Locate and identify every blood parasite.
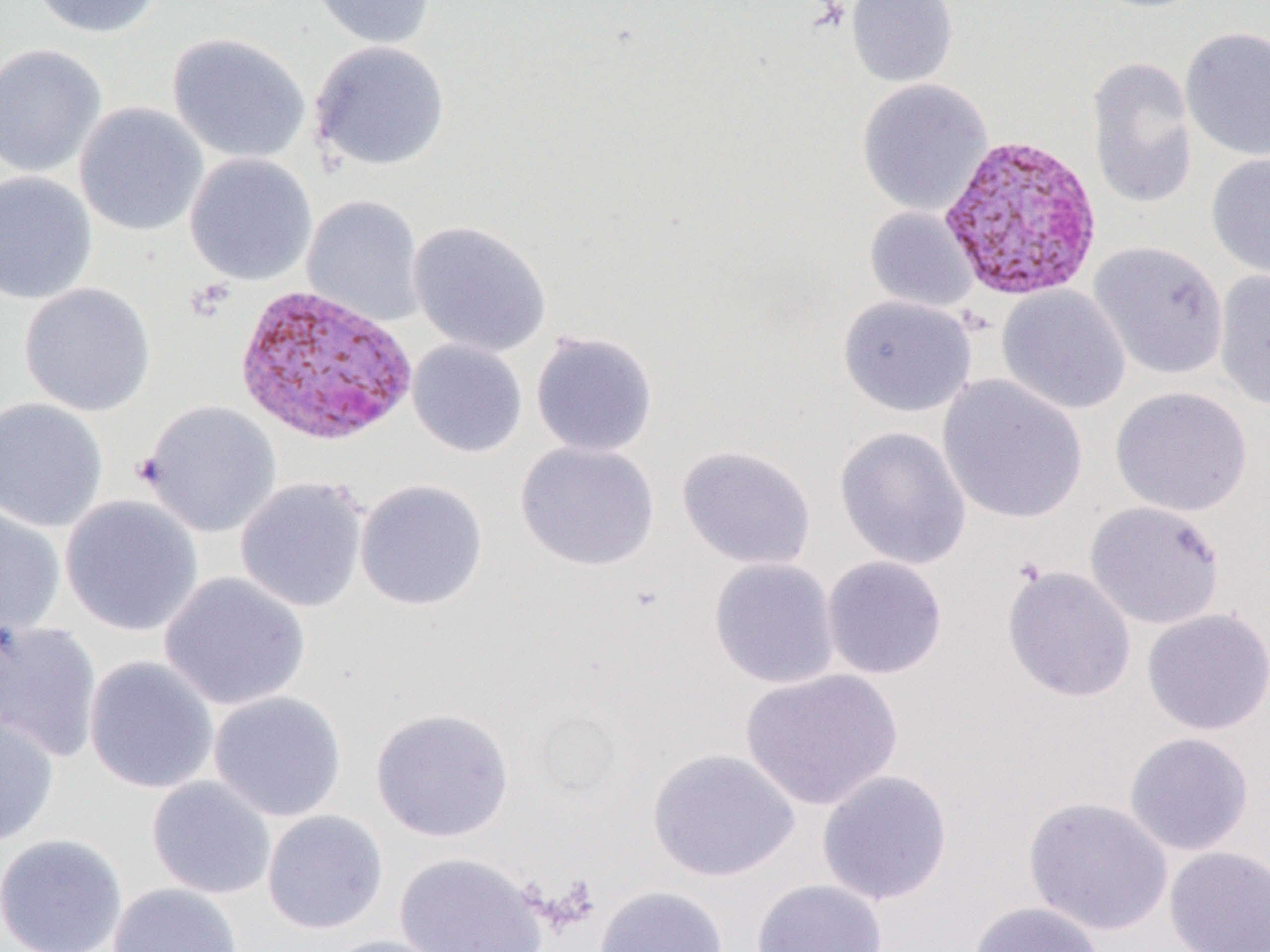

Approximate bounding boxes as [x1, y1, x2, y2] in pixels.
Plasmodium vivax-infected red blood cells: [938, 134, 1103, 300], [232, 282, 419, 448].
No Plasmodium falciparum, Plasmodium ovale, Plasmodium malariae, Babesia divergens, or Trypanosoma brucei observed.

slide-level diagnosis = Plasmodium vivax
field of view = one of a larger specimen
image size = 1270×952 pixels
uninfected red blood cell locations = approximate bounding boxes as [x1, y1, x2, y2] in pixels: [29, 0, 164, 39], [306, 0, 437, 50], [846, 0, 959, 88], [1180, 27, 1270, 162], [166, 32, 311, 164], [308, 40, 450, 172], [0, 42, 107, 178], [1086, 56, 1198, 210], [856, 78, 993, 216], [74, 102, 209, 237], [184, 152, 318, 285], [1205, 152, 1270, 282], [0, 171, 98, 305], [301, 195, 426, 327], [864, 207, 979, 313], [407, 220, 552, 357], [1088, 241, 1229, 379], [1213, 269, 1270, 409], [18, 282, 156, 417], [997, 285, 1131, 415], [838, 295, 978, 417], [530, 330, 659, 458], [407, 339, 528, 458], [937, 374, 1088, 525], [1110, 386, 1252, 517], [0, 397, 109, 533], [138, 400, 282, 537], [834, 425, 971, 570], [515, 441, 660, 571], [677, 444, 816, 570], [235, 477, 369, 613], [354, 479, 488, 612], [59, 495, 204, 637], [1084, 500, 1226, 630], [0, 505, 67, 637], [821, 555, 948, 680], [708, 557, 840, 689], [1002, 564, 1136, 704], [159, 571, 311, 711], [1141, 607, 1270, 736], [0, 619, 104, 762], [83, 655, 219, 794], [739, 668, 903, 811], [208, 690, 347, 822], [369, 706, 515, 842], [0, 709, 59, 848], [1123, 732, 1255, 856], [647, 747, 800, 882], [816, 769, 953, 906], [146, 776, 276, 899], [1024, 796, 1174, 936], [261, 809, 389, 935], [0, 833, 128, 952], [1164, 845, 1270, 951], [393, 851, 550, 952], [752, 878, 888, 952], [107, 882, 243, 952], [593, 885, 730, 952], [967, 900, 1106, 952], [320, 934, 456, 952]
magnification = 1000x
modality = light microscopy
preparation = thin blood smear